Outline each blood parasite and name the species.
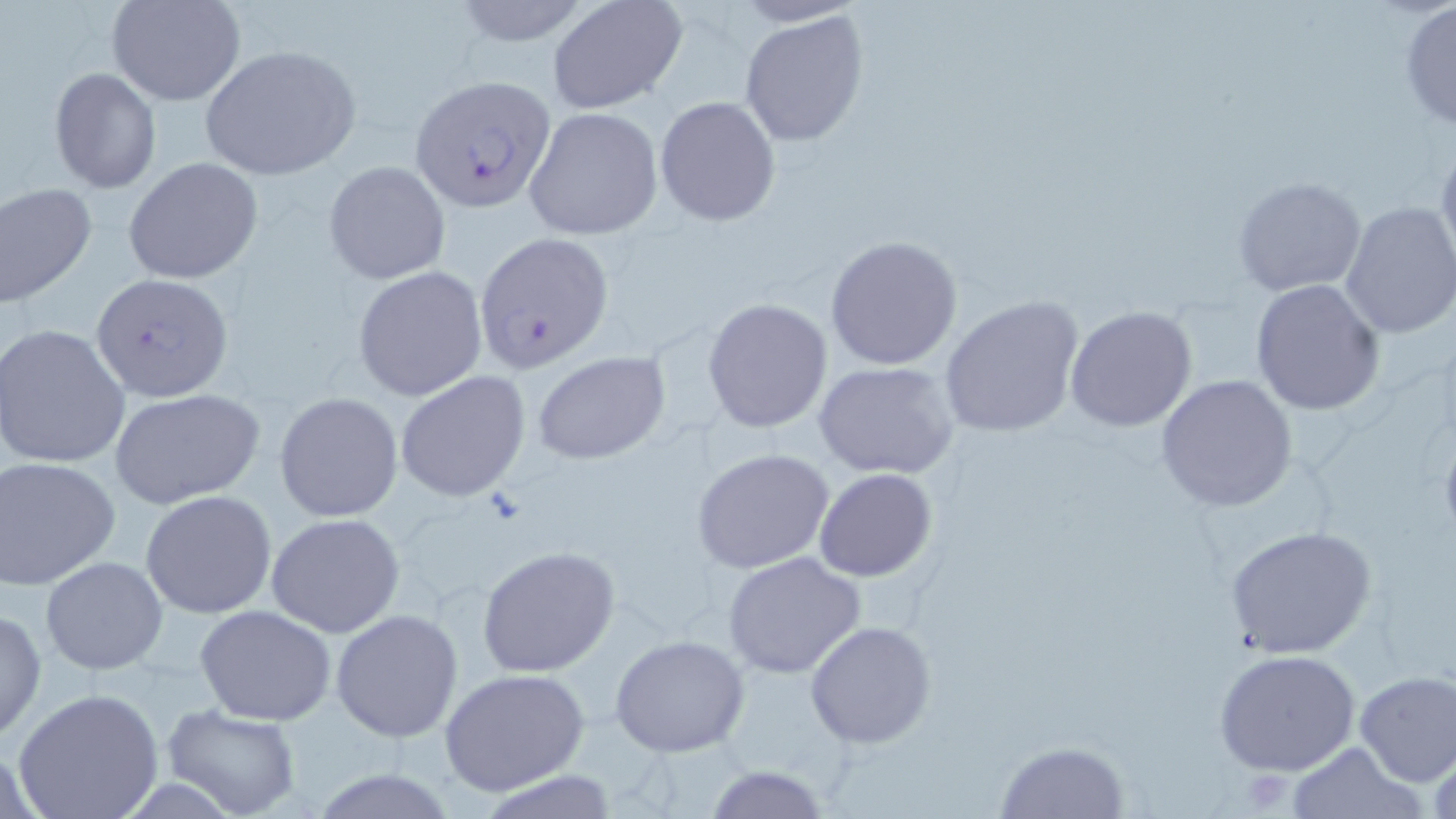

Approximate bounding boxes as named x1/y1/x2/y2 corners in pixels.
Plasmodium falciparum-infected red blood cells: (x1=409, y1=73, x2=558, y2=214), (x1=473, y1=232, x2=615, y2=371), (x1=90, y1=273, x2=234, y2=400).
No Plasmodium ovale, Plasmodium malariae, Plasmodium vivax, Babesia divergens, or Trypanosoma brucei observed.

Summary:
  - Uninfected red blood cell locations: (x1=106, y1=0, x2=246, y2=105), (x1=443, y1=0, x2=597, y2=50), (x1=547, y1=0, x2=689, y2=114), (x1=1398, y1=3, x2=1456, y2=132), (x1=738, y1=9, x2=871, y2=149), (x1=197, y1=44, x2=361, y2=180), (x1=49, y1=68, x2=161, y2=194), (x1=654, y1=95, x2=781, y2=225), (x1=522, y1=106, x2=663, y2=240), (x1=1435, y1=138, x2=1456, y2=276), (x1=124, y1=158, x2=264, y2=284), (x1=323, y1=162, x2=451, y2=284), (x1=1232, y1=175, x2=1365, y2=296), (x1=1, y1=182, x2=97, y2=311), (x1=1337, y1=200, x2=1456, y2=341), (x1=825, y1=235, x2=963, y2=370), (x1=352, y1=267, x2=488, y2=400), (x1=1249, y1=278, x2=1385, y2=416), (x1=938, y1=295, x2=1085, y2=439), (x1=703, y1=301, x2=832, y2=434), (x1=1065, y1=305, x2=1198, y2=432), (x1=2, y1=324, x2=131, y2=469), (x1=531, y1=350, x2=670, y2=464), (x1=812, y1=360, x2=960, y2=479), (x1=395, y1=371, x2=532, y2=502), (x1=1155, y1=373, x2=1299, y2=512), (x1=109, y1=387, x2=266, y2=509), (x1=274, y1=392, x2=403, y2=523), (x1=692, y1=448, x2=836, y2=575), (x1=1, y1=455, x2=122, y2=588), (x1=813, y1=468, x2=937, y2=582), (x1=141, y1=489, x2=277, y2=619), (x1=265, y1=513, x2=406, y2=638), (x1=1225, y1=525, x2=1378, y2=660), (x1=476, y1=545, x2=620, y2=677), (x1=722, y1=551, x2=868, y2=679), (x1=40, y1=555, x2=169, y2=675), (x1=194, y1=604, x2=337, y2=725), (x1=0, y1=606, x2=46, y2=742), (x1=331, y1=609, x2=462, y2=742), (x1=805, y1=622, x2=936, y2=749), (x1=609, y1=635, x2=751, y2=757), (x1=1214, y1=648, x2=1360, y2=777), (x1=441, y1=667, x2=590, y2=796), (x1=1353, y1=670, x2=1456, y2=785), (x1=11, y1=688, x2=164, y2=819), (x1=159, y1=703, x2=303, y2=819), (x1=1425, y1=738, x2=1456, y2=817), (x1=992, y1=740, x2=1132, y2=819), (x1=1285, y1=740, x2=1426, y2=818), (x1=701, y1=765, x2=836, y2=819)
  - Slide-level diagnosis: Plasmodium falciparum
  - Modality: light microscopy
  - Magnification: 1000x
  - Image size: 1456×819 pixels
  - Stain: May-Grünwald-Giemsa
  - Preparation: thin blood smear
  - Field of view: single